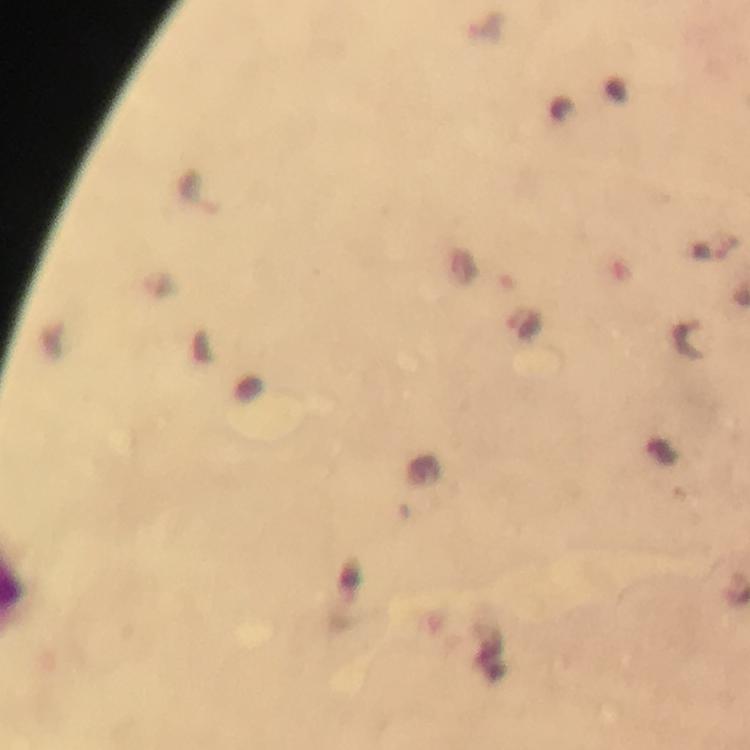

Approximate centers as {x, y} in pixels.
Summary:
  - Malaria parasite locations: {524, 324}, {691, 340}
  - Capture: smartphone photograph through a microscope
  - Magnification: 100x
  - Preparation: thick blood film
  - Stain: Giemsa
  - Image size: 750×750 pixels
  - Cropped from: one field of view
  - Context: from a diagnostic examination for malaria
  - Immersion oil: applied